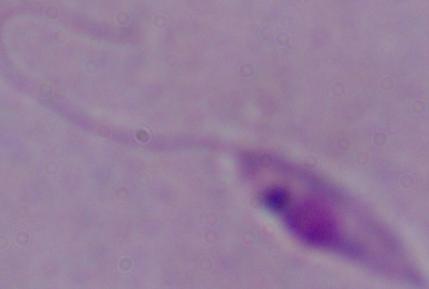

modality = photomicrograph
identification = Leishmania
magnification = 1000x